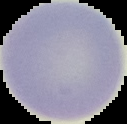 Image is 127×124 pixels. Malaria status: uninfected. Cell region segmented out of the field of view; the surrounding area is masked to black. From a thin blood film.